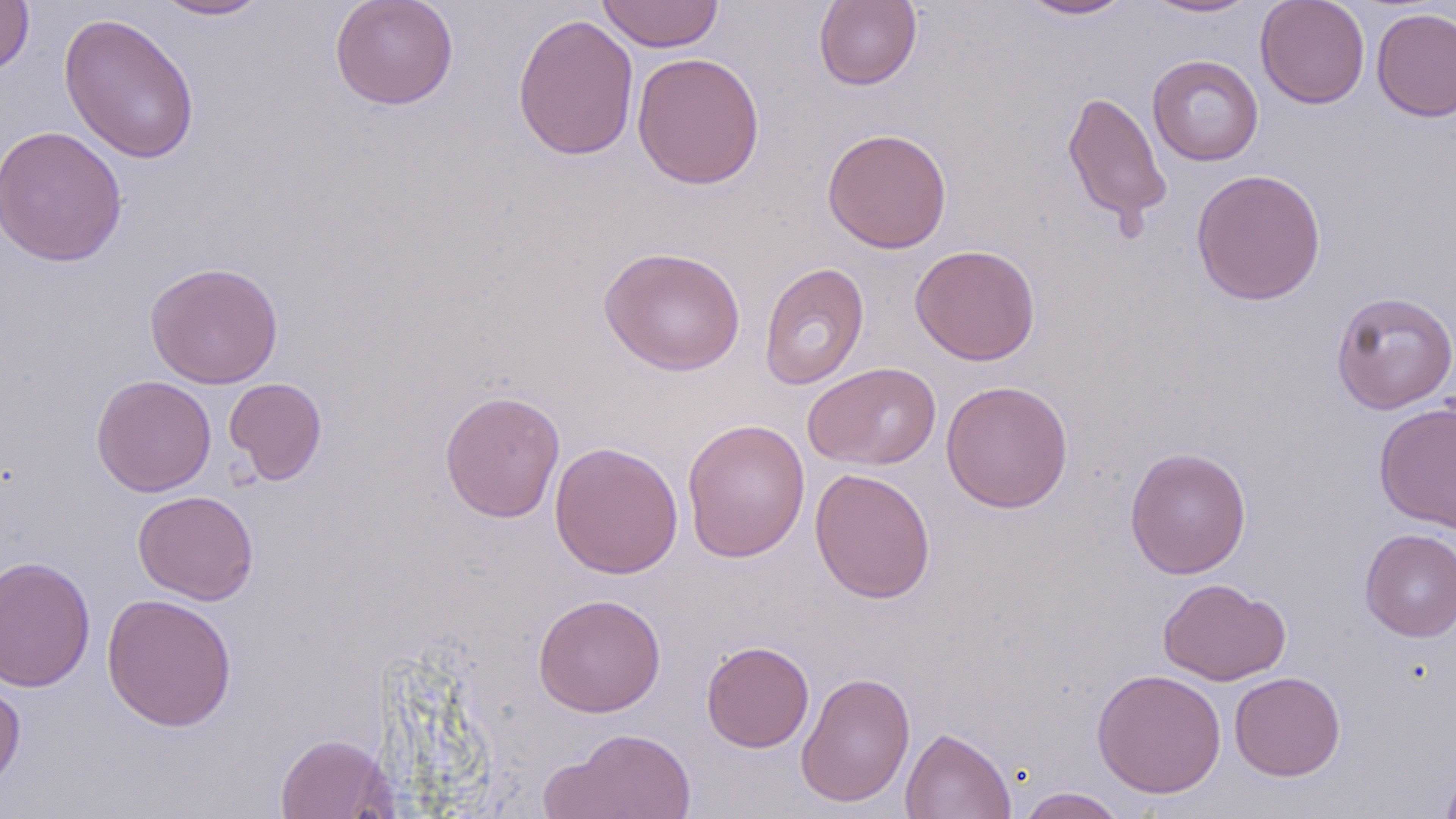

Approximate bounding boxes as named x1/y1/x2/y2 corners in pixels. Uninfected red blood cell locations: (x1=0, y1=0, x2=35, y2=75), (x1=151, y1=0, x2=271, y2=21), (x1=329, y1=0, x2=459, y2=110), (x1=595, y1=0, x2=725, y2=53), (x1=813, y1=0, x2=923, y2=91), (x1=1017, y1=0, x2=1137, y2=20), (x1=1141, y1=0, x2=1260, y2=19), (x1=1255, y1=0, x2=1370, y2=109), (x1=1371, y1=6, x2=1456, y2=122), (x1=59, y1=12, x2=200, y2=164), (x1=512, y1=13, x2=640, y2=161), (x1=632, y1=51, x2=765, y2=190), (x1=1147, y1=55, x2=1264, y2=166), (x1=1062, y1=90, x2=1172, y2=230), (x1=0, y1=124, x2=128, y2=266), (x1=822, y1=127, x2=952, y2=254), (x1=1190, y1=168, x2=1327, y2=306), (x1=910, y1=244, x2=1041, y2=366), (x1=598, y1=246, x2=746, y2=376), (x1=144, y1=262, x2=284, y2=388), (x1=759, y1=262, x2=870, y2=390), (x1=1331, y1=291, x2=1456, y2=415), (x1=803, y1=362, x2=941, y2=470), (x1=91, y1=374, x2=216, y2=497), (x1=224, y1=377, x2=328, y2=485), (x1=940, y1=380, x2=1073, y2=513), (x1=439, y1=389, x2=566, y2=523), (x1=1373, y1=401, x2=1456, y2=533), (x1=681, y1=418, x2=810, y2=563), (x1=549, y1=440, x2=684, y2=580), (x1=1124, y1=446, x2=1251, y2=579), (x1=809, y1=468, x2=936, y2=603), (x1=132, y1=490, x2=259, y2=605), (x1=1360, y1=528, x2=1456, y2=641), (x1=0, y1=555, x2=96, y2=692), (x1=1157, y1=578, x2=1291, y2=686), (x1=101, y1=593, x2=238, y2=731), (x1=533, y1=593, x2=667, y2=718), (x1=701, y1=640, x2=814, y2=753), (x1=1092, y1=668, x2=1227, y2=798), (x1=796, y1=670, x2=916, y2=808), (x1=1228, y1=672, x2=1346, y2=781), (x1=0, y1=674, x2=26, y2=795), (x1=543, y1=727, x2=697, y2=818), (x1=899, y1=727, x2=1016, y2=819), (x1=274, y1=733, x2=394, y2=819), (x1=1439, y1=757, x2=1456, y2=819), (x1=1014, y1=786, x2=1129, y2=818). Slide-level diagnosis: negative for blood parasites. Optical microscopy. One field of a larger specimen. Image is 1456×819 pixels. 1000x magnification. Thin blood film. May-Grünwald-Giemsa stain.